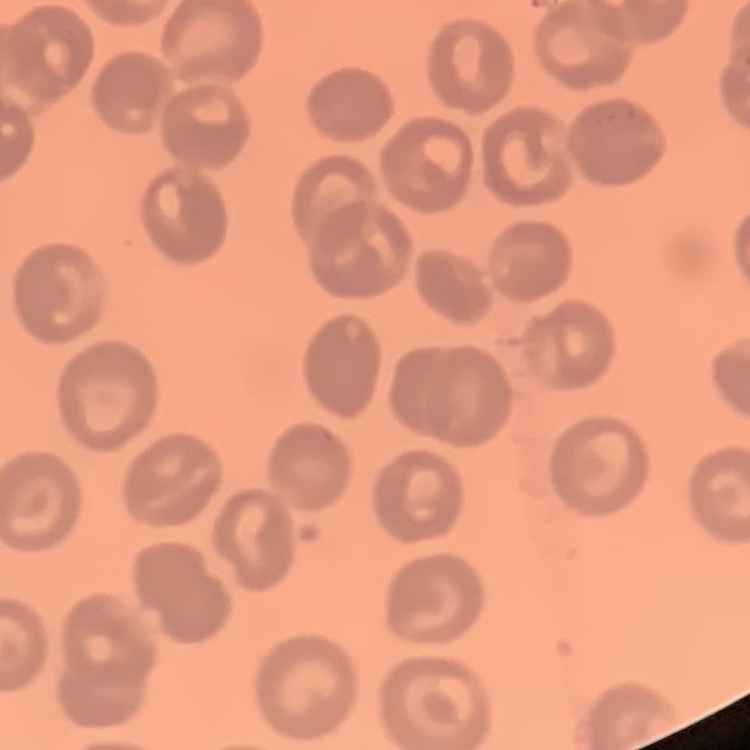

erythrocyte_morphology: no rouleaux formation
preparation: thin peripheral smear
image_type: one tile cut from a larger photomicrograph
stain: Field's or Giemsa